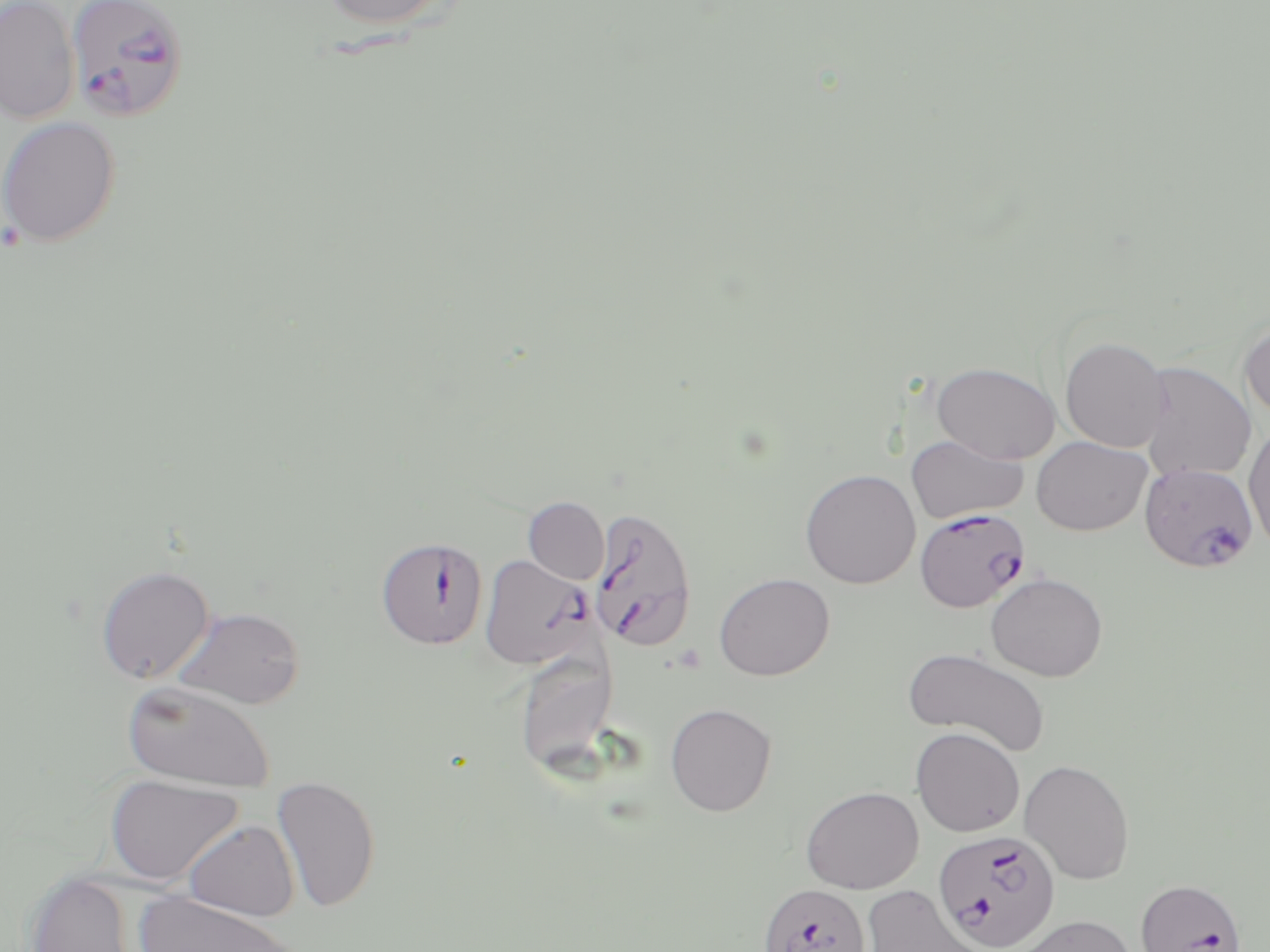
slide_level_diagnosis: Plasmodium falciparum
field_of_view: one of a larger specimen
preparation: thin blood smear
image_size: 1270×952 pixels
modality: optical microscopy
plasmodium_falciparum_infected_red_blood_cell_locations: 'approximate bounding boxes as (x1, y1, x2, y2) in pixels: (68, 2, 191, 129), (1137, 468, 1259, 572), (590, 506, 698, 653), (914, 507, 1030, 612), (375, 536, 488, 649), (480, 554, 594, 669), (932, 829, 1061, 950), (1133, 879, 1247, 952), (757, 883, 870, 951)'
stain: May-Grünwald-Giemsa
magnification: 1000x
uninfected_red_blood_cell_locations: 'approximate bounding boxes as (x1, y1, x2, y2) in pixels: (0, 0, 80, 123), (315, 0, 457, 30), (0, 116, 121, 248), (1239, 318, 1270, 422), (1059, 336, 1171, 452), (1138, 361, 1256, 482), (932, 362, 1061, 465), (1244, 423, 1270, 551), (906, 435, 1028, 524), (1032, 436, 1151, 536), (800, 469, 920, 588), (523, 497, 609, 585), (96, 565, 215, 685), (714, 572, 834, 681), (986, 572, 1108, 681), (172, 606, 306, 710), (905, 646, 1051, 756), (513, 647, 618, 774), (122, 680, 275, 792), (665, 703, 777, 816), (911, 727, 1025, 837), (1019, 759, 1135, 884), (104, 774, 244, 885), (272, 774, 381, 914), (801, 786, 923, 894), (183, 820, 299, 921), (23, 871, 138, 952), (860, 885, 989, 952), (134, 890, 299, 952), (1010, 914, 1137, 952)'